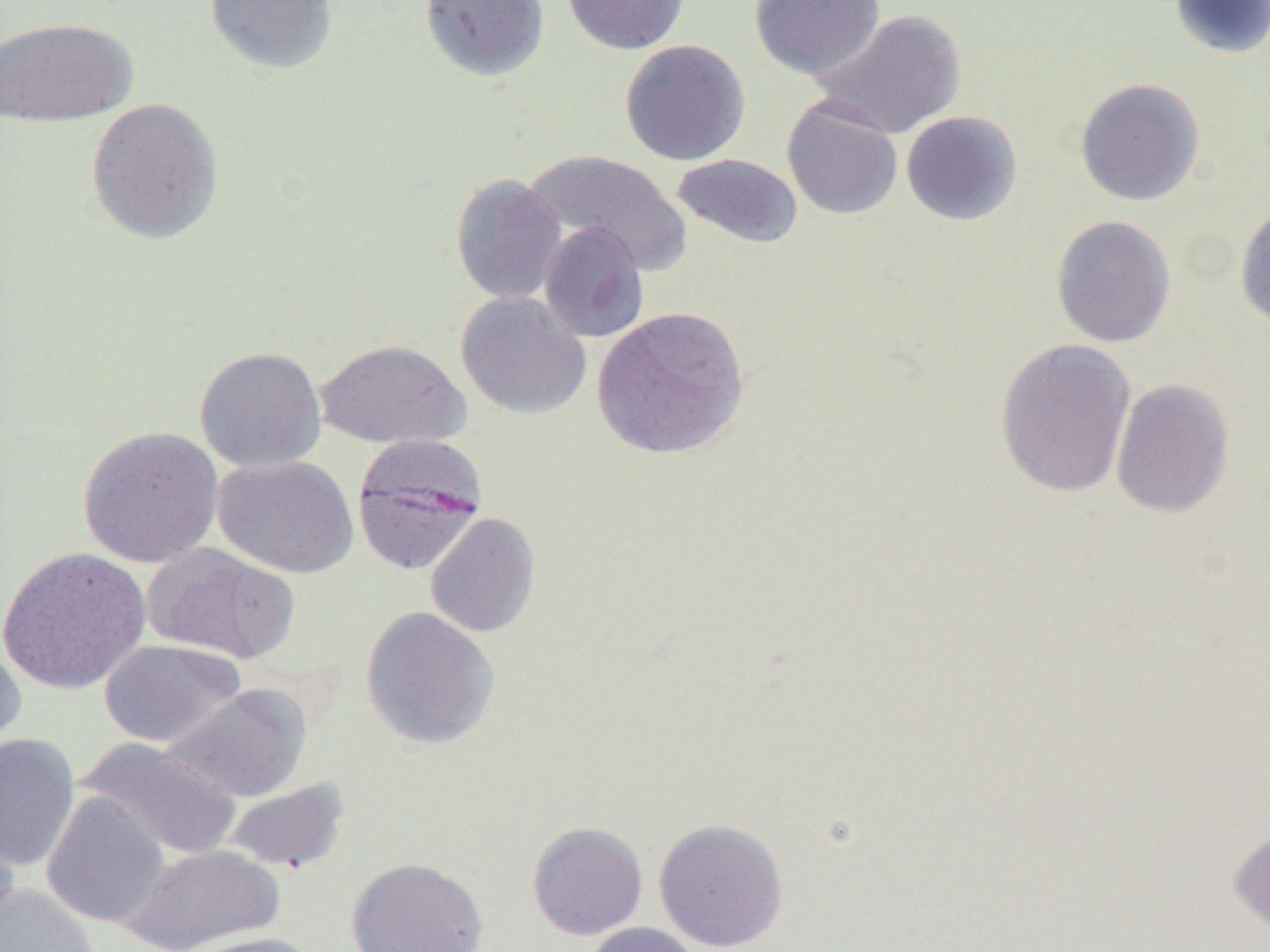

Approximate bounding boxes as (x1,y1)-(x2,y2) corner pairs in pixels. Uninfected red blood cell locations: (203,0)-(339,75), (418,0)-(550,82), (562,0)-(689,54), (749,0)-(885,81), (1168,0)-(1269,59), (811,10)-(966,140), (0,16)-(138,127), (620,39)-(750,166), (1074,78)-(1205,206), (782,97)-(903,220), (86,98)-(225,244), (900,110)-(1023,226), (523,148)-(692,274), (670,153)-(804,250), (450,173)-(567,305), (1235,201)-(1270,333), (1050,215)-(1176,348), (538,221)-(649,343), (456,291)-(592,419), (591,306)-(750,460), (313,338)-(470,449), (994,339)-(1136,498), (194,346)-(326,473), (1110,378)-(1234,518), (77,426)-(224,568), (212,455)-(359,579), (425,512)-(541,638), (143,544)-(299,665), (0,547)-(152,694), (360,606)-(500,750), (98,639)-(244,748), (0,641)-(27,762), (162,683)-(312,803), (0,733)-(79,871), (76,737)-(243,861), (221,778)-(351,874), (41,791)-(170,929), (0,812)-(20,932), (653,818)-(789,952), (527,821)-(648,940), (1229,823)-(1270,937), (121,843)-(285,952), (346,856)-(488,952), (0,883)-(100,952), (582,922)-(703,952), (179,931)-(322,952). Plasmodium malariae-infected red blood cell locations: (350,434)-(488,576). Slide-level diagnosis: Plasmodium malariae. Thin blood film. Image is 1270×952 pixels. One field of a larger specimen. Captured at 1000x magnification. Optical microscopy.